Locate every Plasmodium falciparum-infected red blood cell.
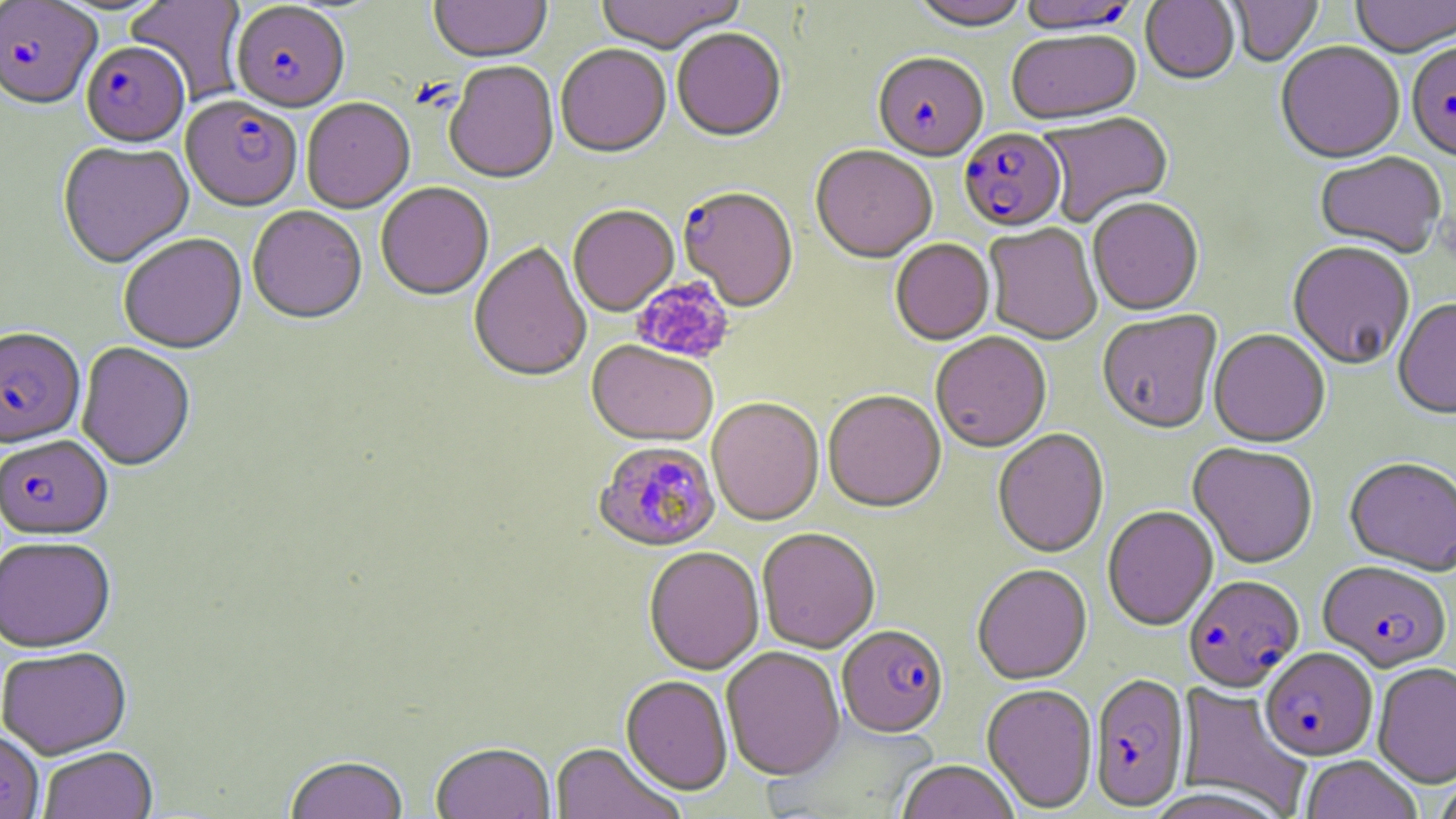

Approximate bounding boxes as [x1, y1, x2, y2] in pixels.
Plasmodium falciparum-infected red blood cells: [1017, 0, 1139, 37], [1, 1, 101, 114], [230, 3, 350, 116], [81, 45, 190, 150], [1407, 45, 1456, 164], [873, 55, 988, 164], [180, 98, 302, 215], [959, 130, 1067, 235], [682, 193, 803, 317], [0, 329, 85, 451], [0, 437, 114, 542], [593, 442, 720, 554], [1318, 562, 1452, 674], [1183, 576, 1305, 694], [837, 626, 949, 739], [1260, 649, 1378, 762], [1089, 675, 1190, 812].

{
  "slide_level_diagnosis": "Plasmodium falciparum",
  "uninfected_red_blood_cell_locations": "approximate bounding boxes as [x1, y1, x2, y2] in pixels: [125, 0, 248, 105], [429, 0, 551, 66], [595, 0, 747, 56], [909, 0, 1032, 34], [1227, 0, 1324, 67], [1352, 0, 1456, 59], [1140, 1, 1240, 87], [672, 30, 787, 144], [1007, 32, 1141, 127], [1276, 44, 1405, 167], [556, 47, 671, 161], [444, 62, 559, 187], [302, 100, 415, 215], [1039, 113, 1175, 227], [57, 143, 194, 271], [811, 146, 936, 266], [1315, 153, 1446, 260], [376, 185, 493, 302], [1087, 200, 1204, 317], [568, 206, 679, 318], [247, 208, 367, 327], [984, 225, 1102, 346], [115, 227, 364, 340], [119, 236, 246, 356], [890, 241, 995, 347], [468, 243, 592, 385], [1287, 243, 1415, 371], [1393, 300, 1456, 422], [1097, 312, 1222, 435], [1208, 331, 1330, 449], [931, 334, 1052, 453], [586, 341, 718, 448], [77, 344, 195, 473], [823, 392, 946, 515], [707, 398, 823, 527], [992, 430, 1109, 560], [1188, 443, 1319, 570], [1344, 459, 1456, 579], [1103, 507, 1219, 633], [757, 529, 880, 653], [0, 539, 116, 655], [643, 548, 764, 676], [972, 566, 1093, 686], [721, 647, 845, 782], [1, 648, 132, 760], [1373, 662, 1456, 789], [620, 676, 733, 796], [1175, 683, 1312, 816], [981, 685, 1098, 814], [0, 731, 43, 819], [549, 743, 685, 819], [431, 745, 555, 819], [39, 747, 158, 819], [1301, 757, 1422, 819], [285, 758, 409, 819], [895, 762, 1020, 819], [1432, 774, 1456, 819]",
  "image_size": "1456×819 pixels",
  "preparation": "thin blood smear",
  "platelet_locations": "approximate bounding boxes as [x1, y1, x2, y2] in pixels: [632, 277, 734, 364]",
  "stain": "May-Grünwald-Giemsa",
  "modality": "light microscopy",
  "field_of_view": "single",
  "magnification": "1000x"
}